Point out each leukocyte.
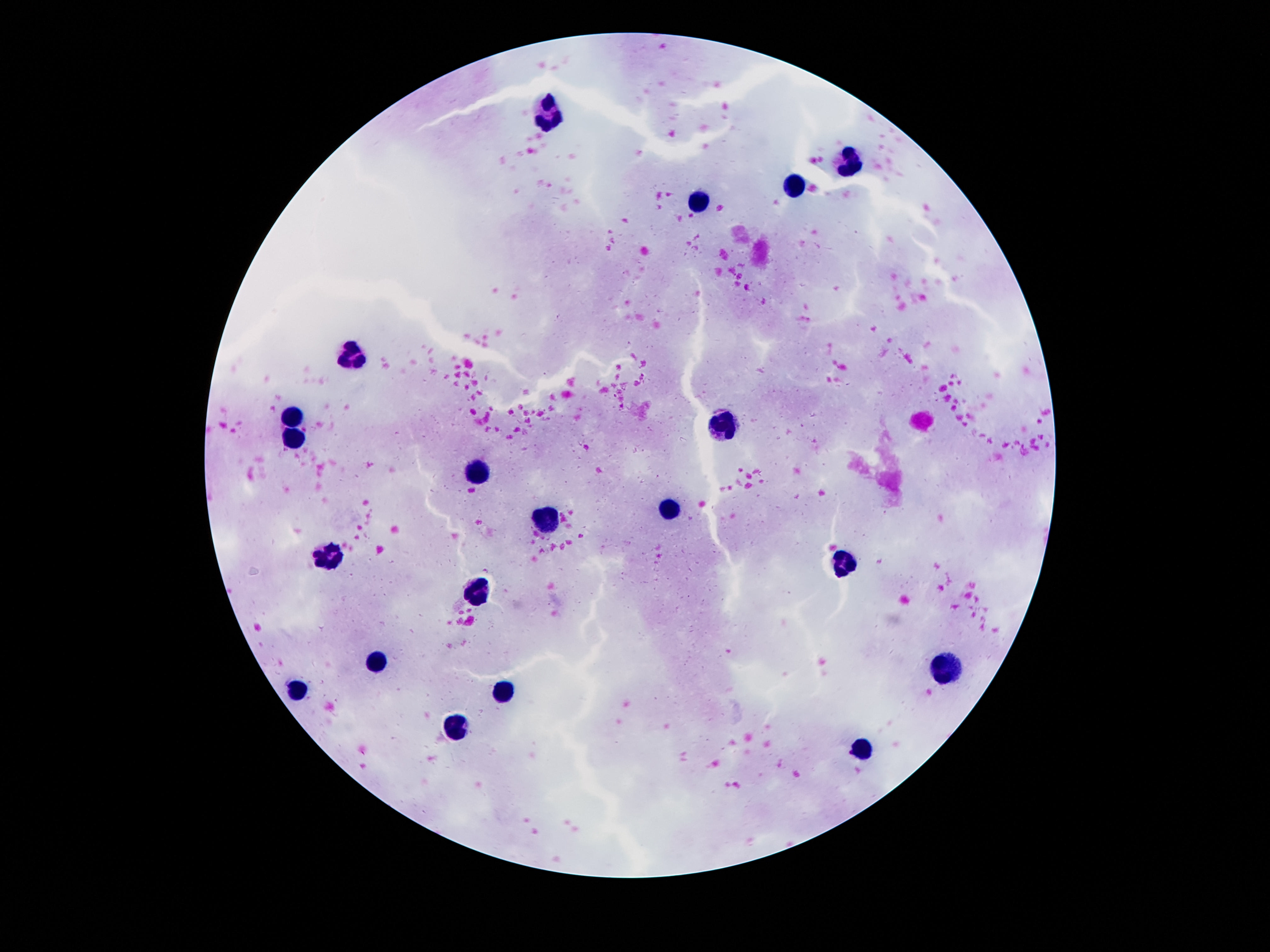

Approximate object centers, in pixels from the top-left corner.
Leukocytes: (x=550, y=111), (x=849, y=162), (x=793, y=186), (x=698, y=202), (x=350, y=354), (x=296, y=415), (x=724, y=427), (x=296, y=438), (x=477, y=473), (x=670, y=510), (x=548, y=520), (x=324, y=553), (x=841, y=561), (x=475, y=597), (x=376, y=665), (x=940, y=672), (x=503, y=690), (x=296, y=692), (x=460, y=727), (x=858, y=748).

{
  "magnification": "100x",
  "capture": "smartphone camera through the microscope eyepiece",
  "field_of_view": "one from this slide",
  "image_size": "1270×952 pixels",
  "patient_malaria_status": "uninfected",
  "preparation": "thick blood film",
  "stain": "Giemsa"
}